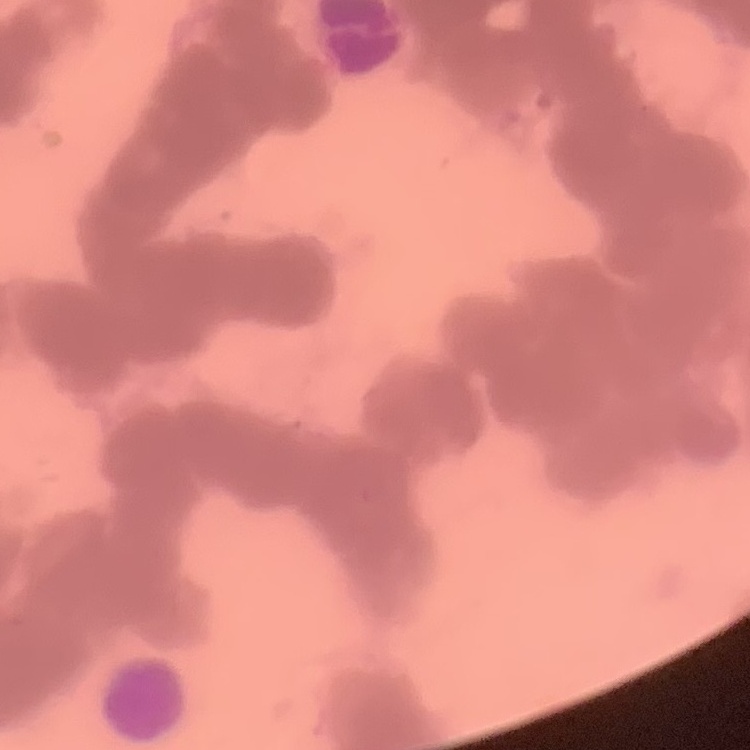
red_blood_cell_morphology: rouleaux formation
image_type: square crop of a larger photomicrograph
stain: Field's or Giemsa
preparation: thin blood smear